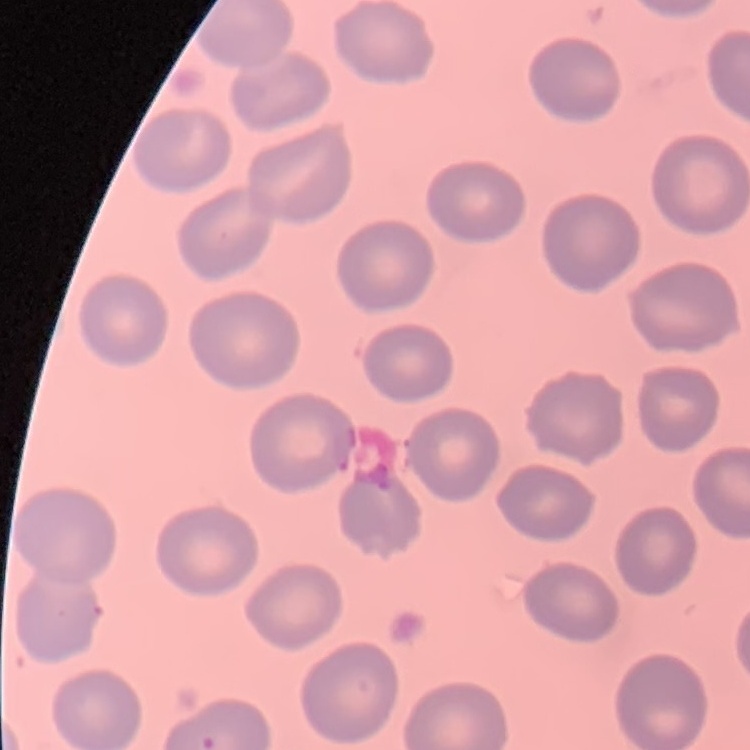 The erythrocytes show no rouleaux formation. One tile cut from a larger photomicrograph. Field's or Giemsa stain. Thin peripheral smear.